Assess the morphology of the erythrocytes.
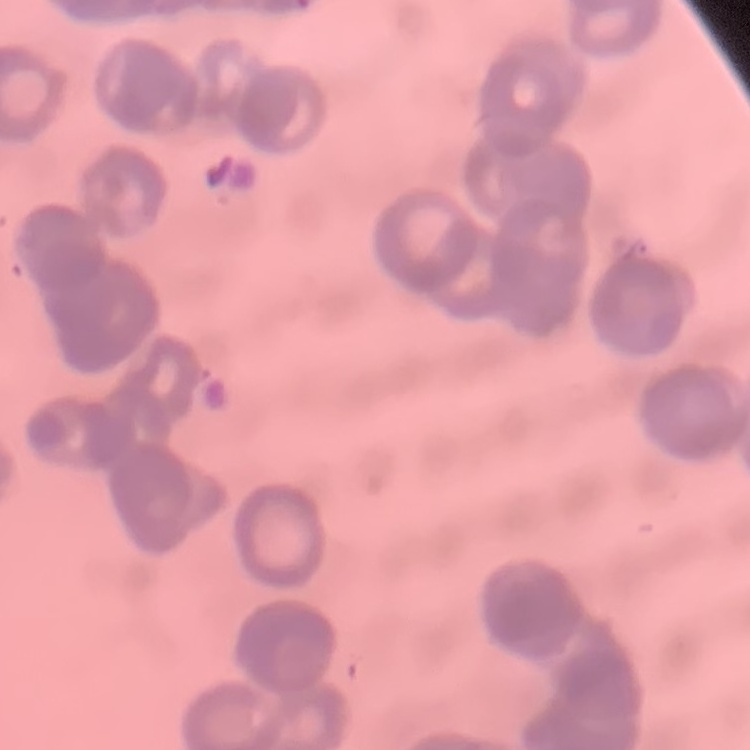

They show rouleaux formation.

image type = square crop of a larger photomicrograph
preparation = thin blood smear
stain = Field's or Giemsa